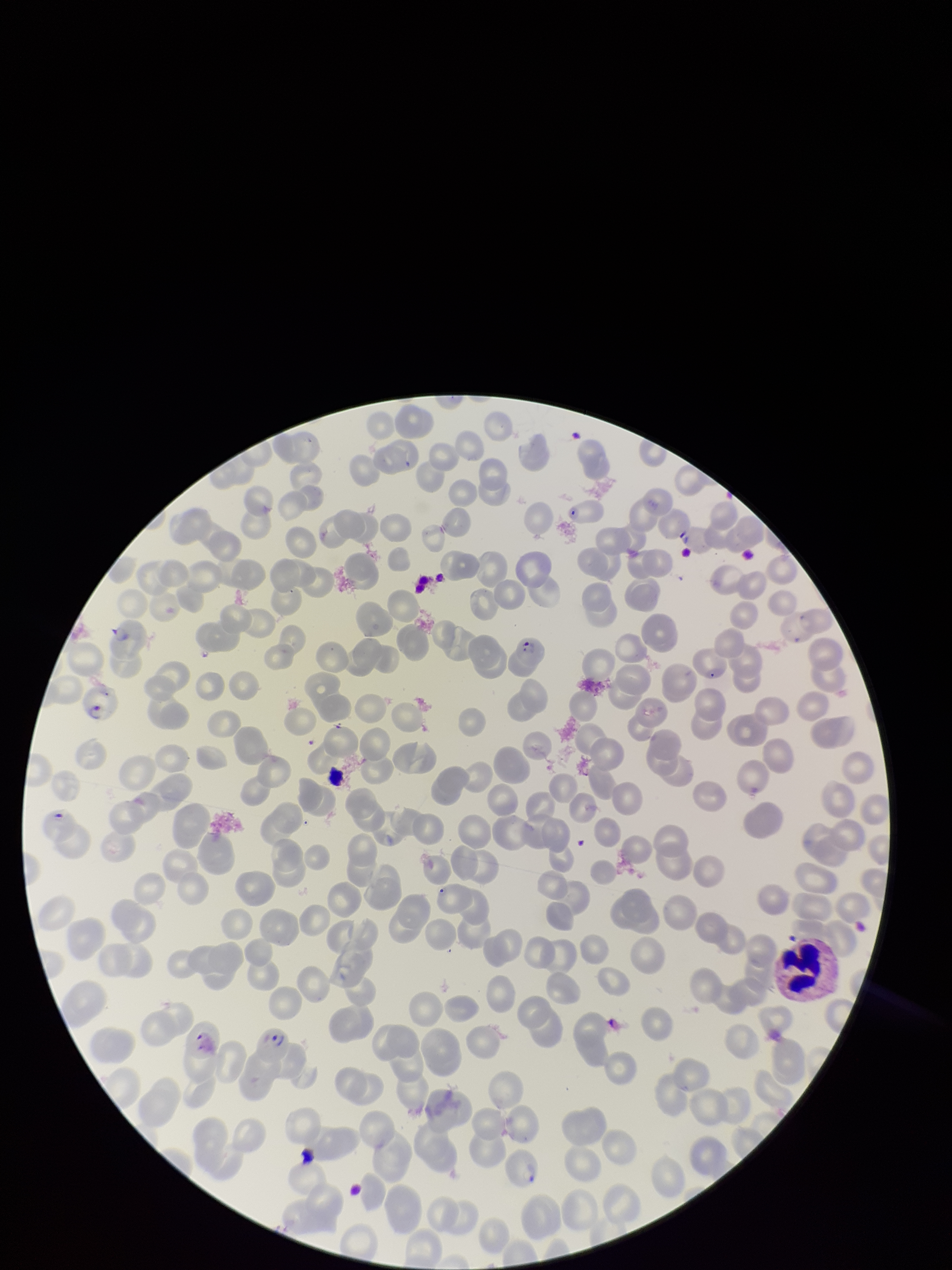

Summary:
  - Species reported for this patient: Plasmodium falciparum
  - Image size: 952×1270 pixels
  - Red blood cell count: 215
  - Patient malaria status: infected
  - Preparation: thin
  - Capture: smartphone photograph through the microscope eyepiece
  - Parasitized red blood cells: seen
  - Field of view: single
  - Parasitized red blood cell count: 3
  - Stain: Giemsa